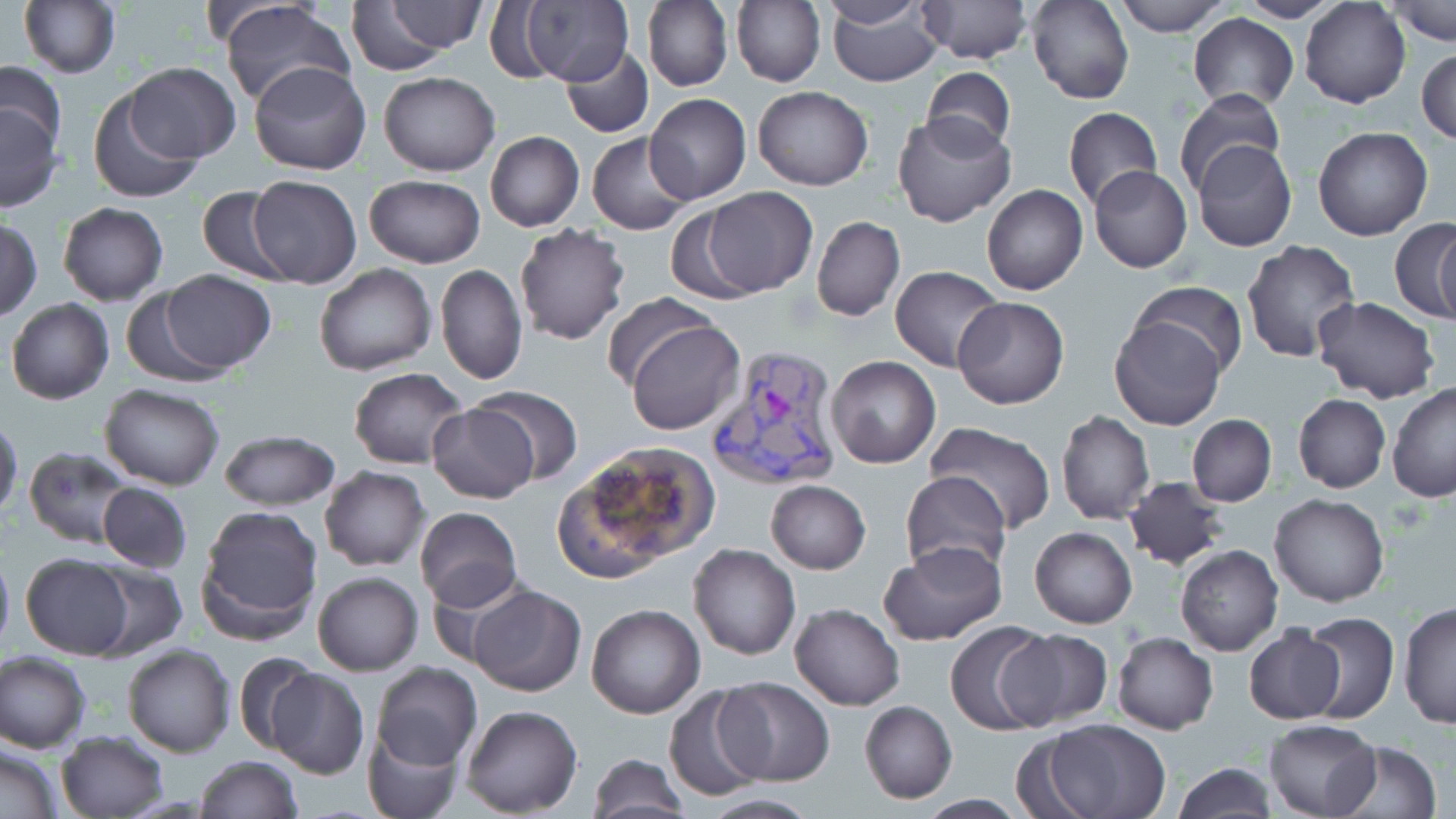 Approximate bounding boxes as [x1, y1, x2, y2] in pixels. Uninfected red blood cell locations: [18, 0, 121, 79], [217, 0, 354, 111], [518, 0, 636, 87], [732, 0, 824, 88], [826, 0, 943, 86], [916, 0, 1032, 66], [1111, 0, 1235, 36], [1235, 0, 1344, 22], [1300, 0, 1410, 108], [1385, 0, 1455, 47], [642, 1, 732, 92], [817, 1, 933, 28], [1026, 1, 1133, 104], [384, 2, 486, 52], [346, 3, 470, 74], [1187, 13, 1299, 111], [559, 46, 653, 139], [1417, 46, 1456, 145], [249, 60, 370, 175], [0, 61, 68, 155], [125, 63, 241, 163], [920, 66, 1017, 157], [379, 70, 499, 176], [751, 86, 873, 191], [1173, 88, 1290, 194], [88, 90, 201, 205], [645, 93, 751, 205], [0, 99, 63, 211], [1063, 106, 1162, 208], [892, 112, 1017, 227], [1313, 127, 1433, 242], [485, 132, 584, 231], [588, 133, 695, 236], [1191, 138, 1298, 253], [1088, 165, 1192, 273], [362, 174, 485, 269], [248, 175, 361, 287], [981, 184, 1088, 296], [195, 185, 295, 283], [699, 187, 817, 296], [58, 202, 168, 305], [664, 206, 768, 305], [812, 215, 905, 322], [1, 217, 41, 321], [1390, 219, 1456, 322], [514, 224, 632, 347], [1432, 226, 1456, 325], [1241, 240, 1363, 364], [313, 264, 437, 377], [436, 264, 526, 386], [890, 265, 1003, 371], [157, 270, 275, 374], [1131, 280, 1248, 378], [120, 289, 232, 389], [603, 292, 717, 392], [952, 296, 1070, 410], [1311, 296, 1440, 405], [5, 297, 115, 405], [1111, 313, 1223, 430], [627, 317, 746, 436], [827, 356, 941, 470], [349, 366, 469, 469], [1387, 383, 1456, 503], [100, 384, 225, 490], [473, 387, 582, 490], [1293, 393, 1389, 493], [428, 401, 539, 504], [1056, 411, 1155, 525], [0, 414, 23, 519], [1187, 415, 1276, 506], [924, 420, 1057, 532], [218, 428, 339, 511], [574, 442, 720, 566], [23, 446, 134, 548], [319, 466, 430, 570], [550, 471, 675, 585], [900, 471, 1012, 580], [1123, 476, 1227, 570], [765, 479, 871, 574], [98, 482, 193, 573], [1269, 494, 1392, 608], [196, 505, 324, 641], [414, 506, 523, 610], [1030, 527, 1138, 629], [878, 542, 1008, 646], [688, 544, 800, 660], [1176, 544, 1283, 655], [0, 545, 14, 659], [21, 553, 135, 659], [86, 564, 187, 660], [422, 568, 531, 668], [313, 571, 423, 675], [467, 585, 586, 696], [1397, 600, 1456, 732], [587, 603, 705, 718], [790, 603, 905, 710], [1298, 610, 1400, 724], [945, 620, 1055, 736], [1242, 624, 1346, 724], [1000, 629, 1112, 731], [1112, 632, 1218, 734], [120, 644, 235, 757], [1, 651, 90, 754], [232, 651, 324, 756], [368, 662, 481, 771], [266, 669, 369, 778], [715, 677, 835, 786], [662, 685, 770, 801], [859, 701, 957, 803], [461, 705, 584, 817], [1036, 717, 1173, 819], [1264, 718, 1381, 817], [362, 727, 461, 819], [55, 730, 168, 818], [1334, 740, 1441, 819], [1, 744, 62, 818], [589, 753, 690, 819], [194, 755, 304, 818], [1172, 763, 1277, 818], [696, 794, 821, 818], [914, 795, 1034, 819]. Plasmodium vivax-infected red blood cell locations: [707, 343, 843, 491]. Slide-level diagnosis: Plasmodium vivax. May-Grünwald-Giemsa stain. One field of a larger specimen. Optical microscopy. Thin blood smear. Image is 1456×819 pixels. 1000x magnification.